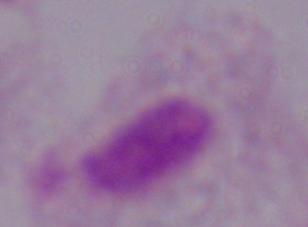
modality = micrograph
identification = trichomonad
magnification = 1000x